Give the extent of all Plasmodium falciparum-infected red blood cells.
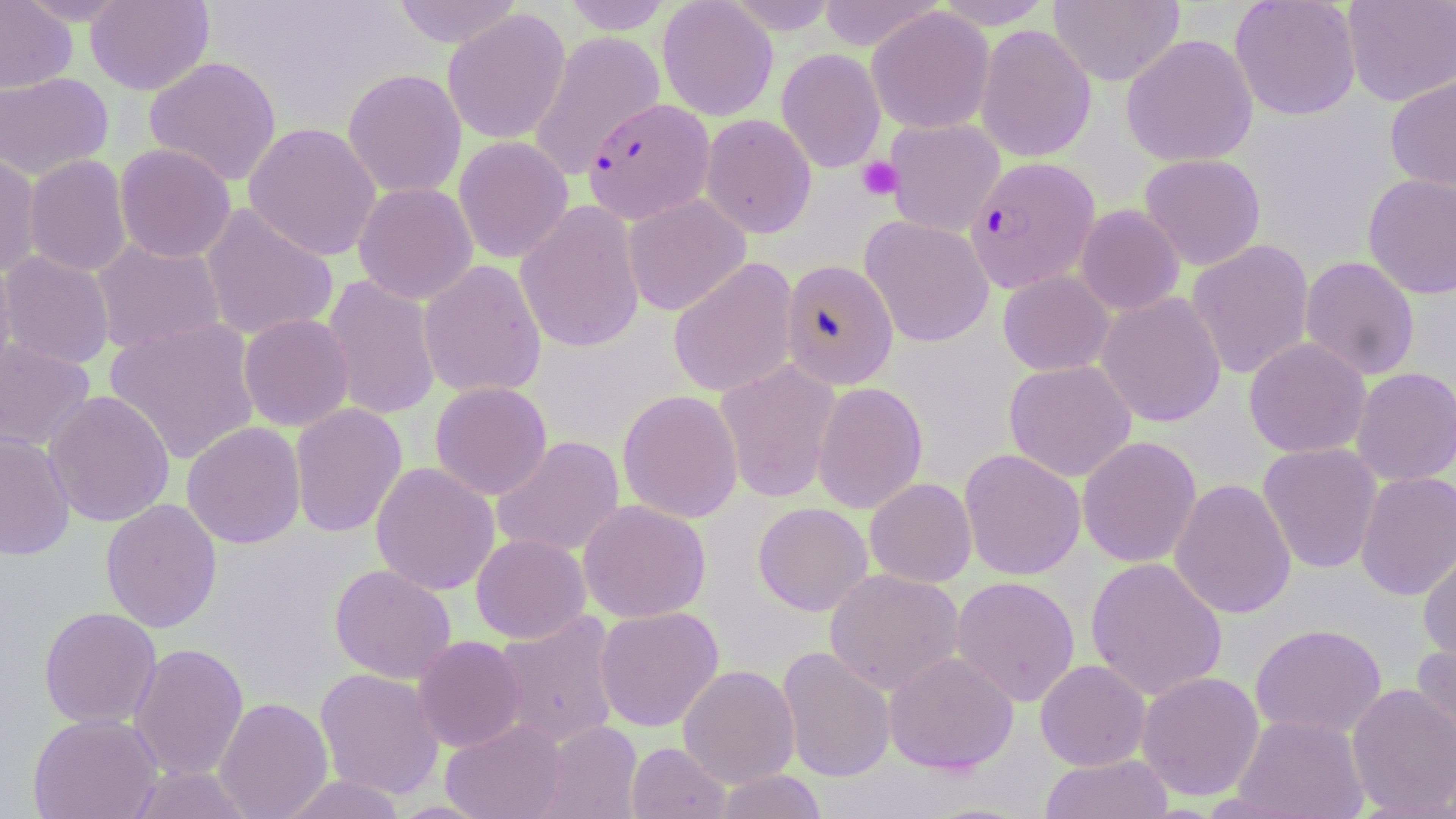

Approximate bounding boxes as [x1, y1, x2, y2] in pixels.
Plasmodium falciparum-infected red blood cells: [583, 98, 714, 224], [964, 156, 1100, 293].

Platelet locations: [856, 156, 903, 201]. Uninfected red blood cell locations: [0, 0, 76, 94], [84, 0, 215, 96], [390, 0, 524, 47], [560, 0, 674, 34], [657, 0, 778, 121], [723, 0, 841, 34], [816, 0, 945, 51], [932, 0, 1055, 29], [1049, 0, 1184, 86], [1229, 0, 1362, 121], [1342, 0, 1456, 107], [867, 6, 994, 134], [442, 9, 571, 145], [975, 24, 1097, 163], [527, 31, 666, 180], [1121, 33, 1258, 167], [776, 48, 885, 173], [143, 55, 282, 186], [342, 68, 467, 198], [0, 71, 114, 181], [1385, 75, 1456, 193], [700, 113, 816, 239], [883, 118, 1005, 237], [243, 122, 382, 261], [453, 136, 573, 264], [114, 143, 236, 263], [0, 149, 42, 277], [1139, 153, 1266, 270], [24, 154, 133, 277], [1362, 173, 1456, 300], [353, 182, 478, 305], [622, 194, 751, 315], [515, 200, 645, 353], [200, 202, 339, 342], [1075, 204, 1185, 316], [859, 215, 994, 348], [90, 237, 226, 355], [1187, 239, 1314, 380], [0, 251, 115, 369], [0, 254, 18, 386], [1300, 256, 1420, 381], [667, 257, 798, 398], [418, 259, 547, 399], [780, 259, 898, 390], [998, 270, 1115, 376], [322, 274, 442, 421], [1095, 291, 1227, 427], [238, 313, 355, 431], [105, 317, 261, 464], [1244, 337, 1371, 458], [0, 338, 96, 452], [715, 359, 840, 504], [1004, 360, 1137, 482], [1351, 367, 1456, 486], [429, 381, 552, 500], [811, 381, 928, 514], [617, 389, 744, 524], [42, 390, 176, 528], [289, 403, 408, 538], [181, 421, 306, 549], [0, 430, 75, 561], [491, 435, 625, 558], [1077, 436, 1201, 568], [1258, 443, 1382, 574], [959, 448, 1086, 580], [370, 462, 500, 596], [1354, 470, 1456, 601], [865, 477, 977, 587], [1169, 478, 1296, 620], [100, 498, 222, 634], [578, 499, 711, 623], [753, 502, 872, 616], [471, 533, 590, 643], [1418, 545, 1456, 666], [1085, 557, 1227, 701], [330, 564, 456, 683], [824, 568, 965, 696], [951, 575, 1080, 707], [38, 606, 162, 729], [594, 606, 724, 732], [492, 611, 622, 748], [1250, 623, 1387, 739], [412, 635, 526, 752], [1411, 642, 1455, 761], [129, 643, 249, 781], [776, 646, 896, 783], [883, 651, 1019, 774], [1035, 659, 1151, 771], [677, 664, 800, 788], [314, 668, 445, 800], [1137, 671, 1264, 801], [1346, 683, 1456, 817], [214, 697, 333, 819], [28, 713, 162, 819], [1233, 715, 1369, 818], [441, 718, 569, 819], [538, 720, 643, 819], [626, 742, 730, 819], [1039, 754, 1174, 819], [126, 764, 256, 819], [711, 769, 829, 819], [276, 774, 408, 818]. Slide-level diagnosis: Plasmodium falciparum. Captured at 1000x magnification. One field of a larger specimen. Image is 1456×819 pixels. May-Grünwald-Giemsa stain. Optical microscopy. Thin blood smear.